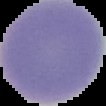
The area outside the segmented cell region is set to black. Image is 106×106 pixels. Malaria status: uninfected. From a thin blood smear.